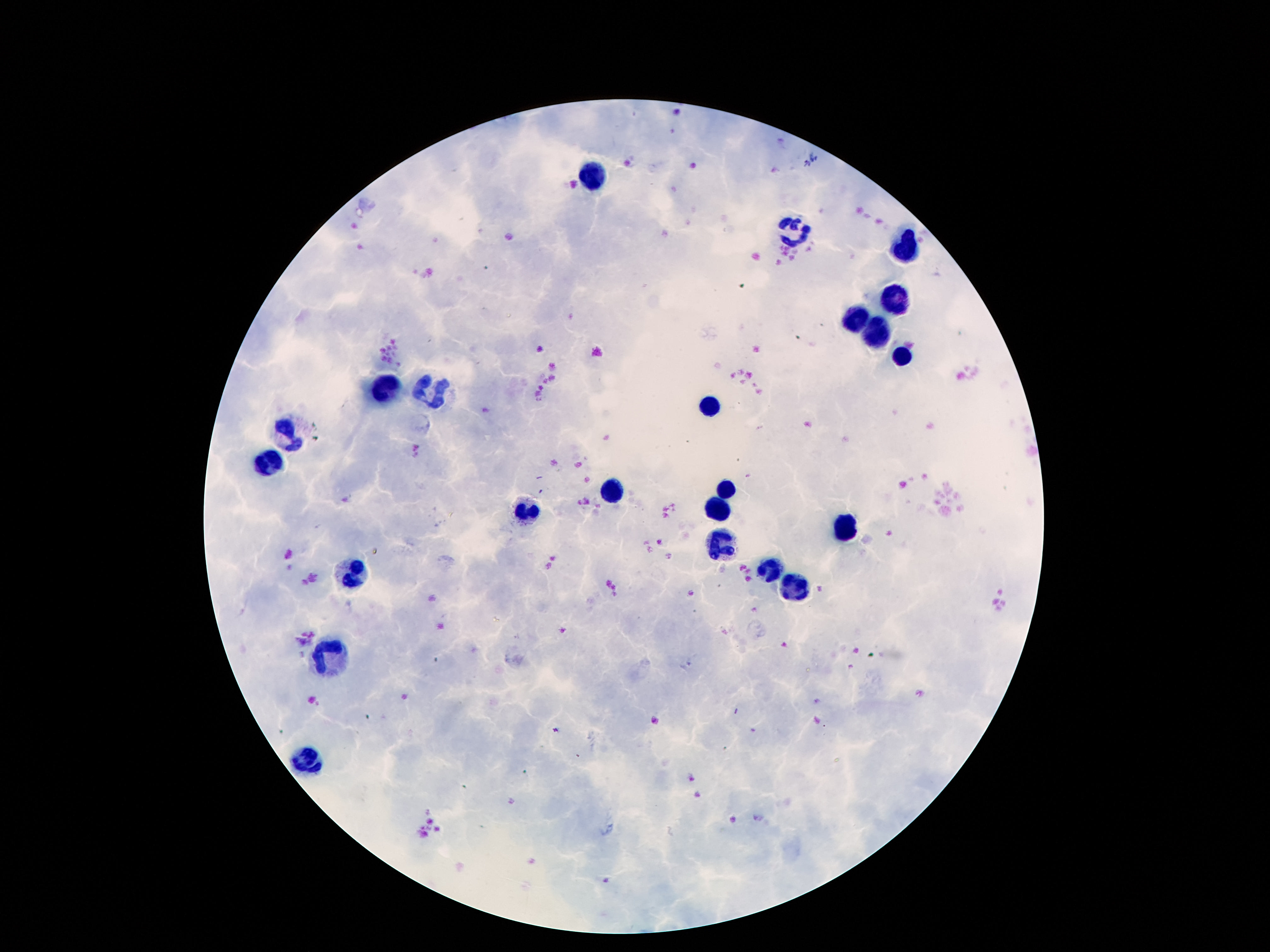
Approximate object centers, in pixels from the top-left corner. Leukocyte locations: (x=593, y=175), (x=792, y=235), (x=904, y=244), (x=894, y=294), (x=853, y=322), (x=878, y=336), (x=900, y=355), (x=437, y=390), (x=386, y=392), (x=710, y=405), (x=290, y=433), (x=271, y=467), (x=726, y=488), (x=611, y=489), (x=722, y=509), (x=527, y=510), (x=847, y=530), (x=720, y=545), (x=771, y=567), (x=353, y=575), (x=792, y=586), (x=335, y=652), (x=306, y=756). Single field of view. 100x magnification. Thick peripheral-blood smear. Giemsa stain. Patient malaria status: negative. Photographed through the microscope eyepiece with a smartphone camera. Image is 1270×952 pixels.